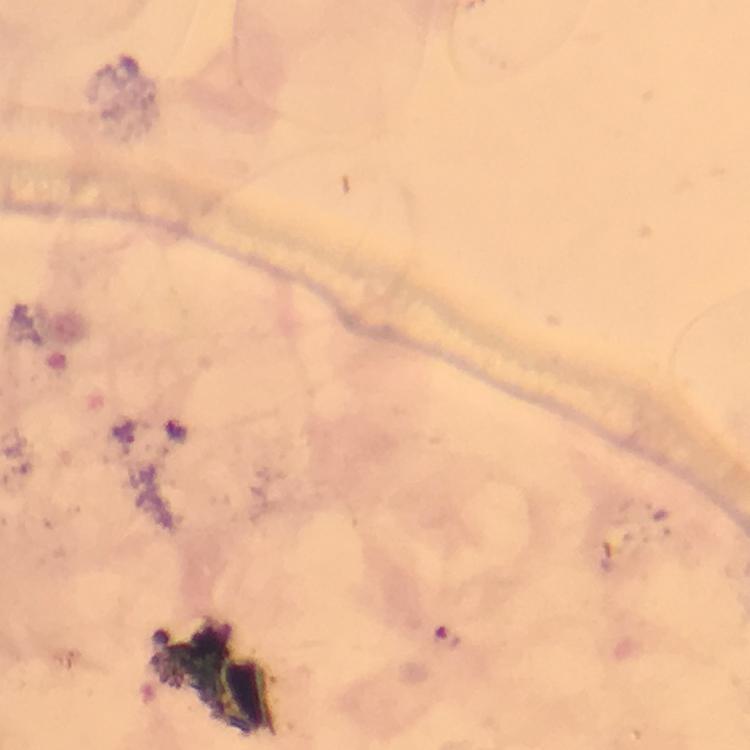

Approximate centers as [x, y] in pixels.
Summary:
  - Malaria parasite locations: [127, 430]
  - Stain: Giemsa
  - Magnification: 100x
  - Context: from a malaria diagnostic workup
  - Cropped from: one field of view
  - Image size: 750×750 pixels
  - Immersion oil: applied
  - Preparation: thick blood film
  - Capture: smartphone camera through the microscope